Outline each Plasmodium falciparum-infected red blood cell.
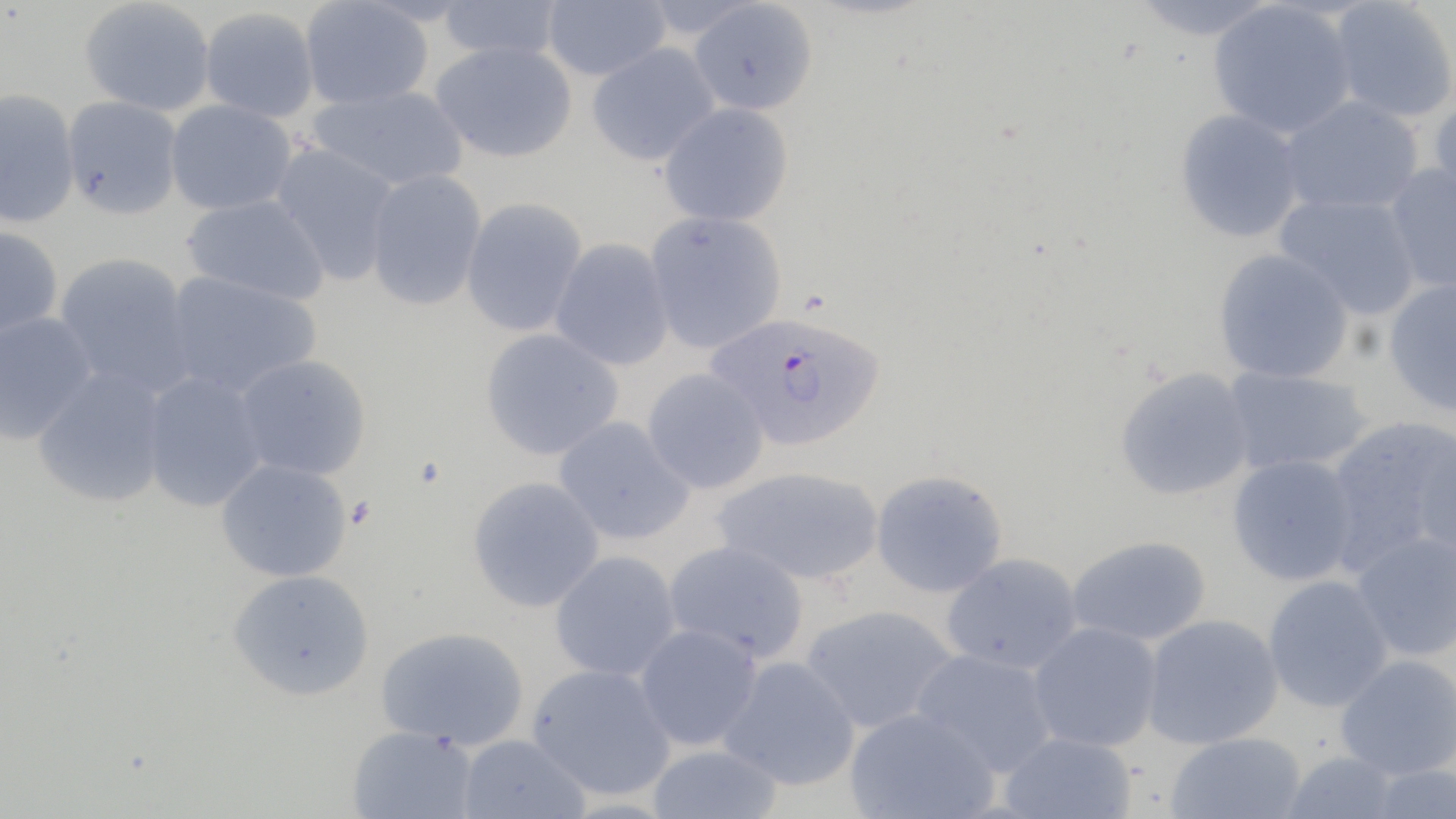

Approximate bounding boxes as (x1,y1)-(x2,y2) corner pairs in pixels.
Plasmodium falciparum-infected red blood cells: (708,311)-(886,451).

slide-level diagnosis = Plasmodium falciparum
field of view = single
magnification = 1000x
image size = 1456×819 pixels
uninfected red blood cell locations = approximate bounding boxes as (x1,y1)-(x2,y2) corner pairs in pixels: (80,0)-(216,117), (436,0)-(566,63), (541,0)-(671,81), (1129,0)-(1282,42), (1328,0)-(1456,123), (299,1)-(434,111), (688,1)-(818,116), (1208,2)-(1356,139), (199,7)-(319,123), (431,41)-(578,163), (586,42)-(720,167), (306,84)-(470,192), (0,88)-(80,230), (61,95)-(184,221), (1279,95)-(1424,216), (1429,95)-(1456,219), (165,99)-(298,216), (657,102)-(794,227), (1173,109)-(1305,243), (269,142)-(401,287), (1382,163)-(1456,297), (364,169)-(488,312), (1275,193)-(1423,321), (181,194)-(330,305), (460,197)-(589,338), (645,210)-(787,354), (0,225)-(63,341), (550,239)-(674,372), (1212,248)-(1355,384), (53,252)-(198,399), (161,270)-(323,400), (1383,278)-(1456,417), (0,311)-(97,446), (480,328)-(624,461), (233,354)-(372,481), (32,365)-(171,508), (1114,366)-(1255,501), (1221,366)-(1374,477), (642,368)-(769,495), (140,369)-(269,512), (1323,415)-(1456,573), (553,416)-(696,546), (1411,434)-(1456,562), (1226,453)-(1360,587), (215,459)-(352,583), (712,465)-(885,585), (870,469)-(1008,598), (466,476)-(604,613), (1350,530)-(1456,662), (1066,535)-(1213,646), (663,540)-(809,664), (549,550)-(682,682), (941,552)-(1083,675), (227,568)-(375,701), (1262,574)-(1394,713), (800,604)-(959,735), (1141,613)-(1284,750), (1028,621)-(1163,752), (634,624)-(763,751), (374,626)-(530,752), (911,648)-(1059,778), (1334,654)-(1456,780), (717,655)-(861,792), (526,664)-(676,802), (844,708)-(999,819), (346,724)-(479,819), (998,731)-(1137,819), (1163,731)-(1307,819), (457,734)-(590,819), (645,743)-(784,819), (1278,750)-(1402,819), (1365,763)-(1455,818)
preparation = thin blood smear
modality = optical microscopy
stain = May-Grünwald-Giemsa